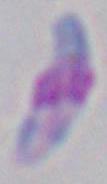
magnification = 1000x
identification = Toxoplasma gondii
modality = micrograph